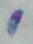
1000x magnification. Toxoplasma gondii is seen. Photomicrograph.